Classify this cell by malaria status.
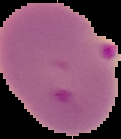

Parasitized.

image size = 121×139 pixels
preparation = thin blood smear
image type = segmented cell region with the area outside set to black